Identify the cell.
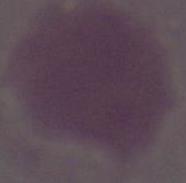
This is an erythrocyte.

Photomicrograph. 1000x magnification.